Locate every blood parasite and identify its species.
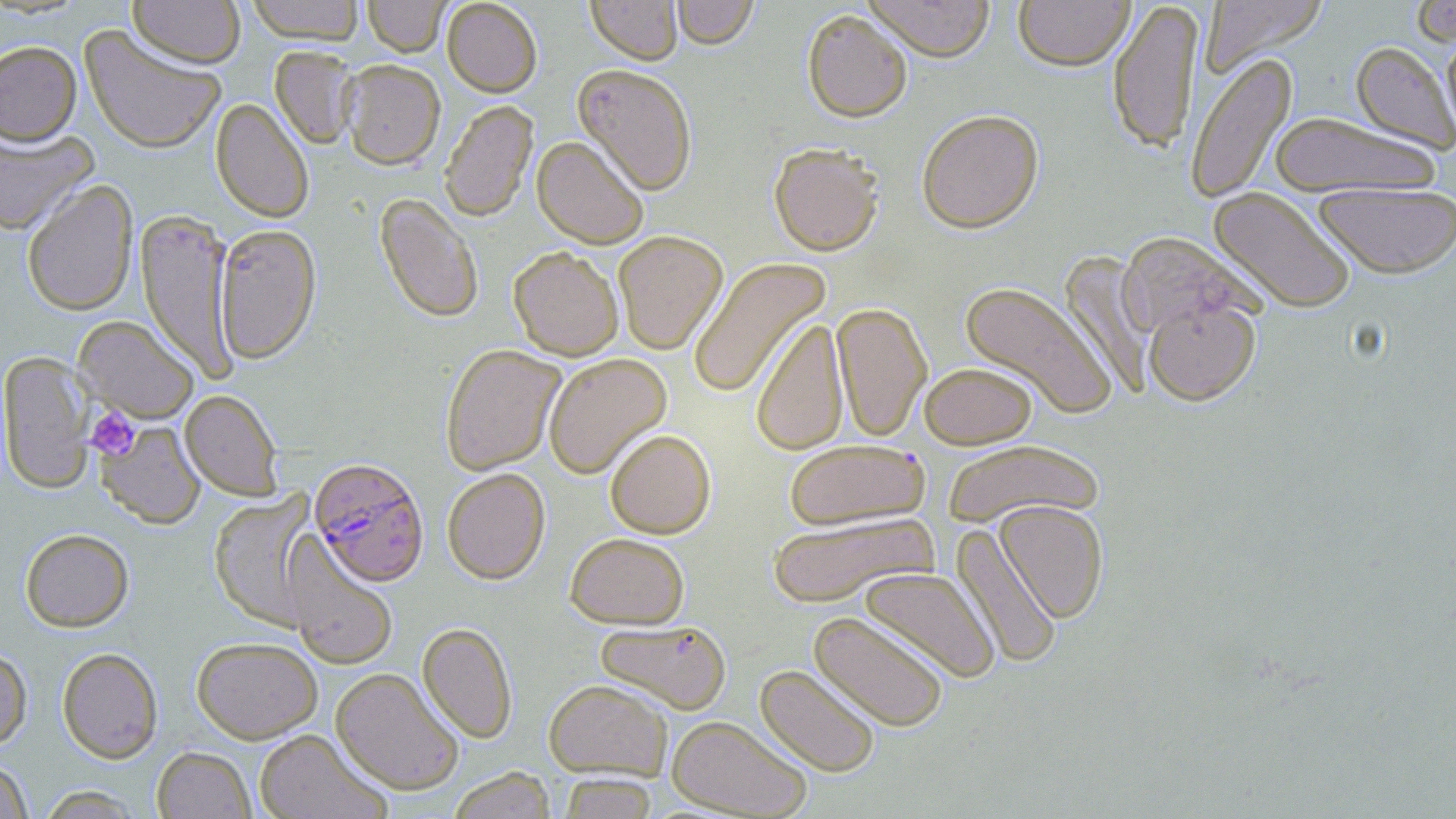
Approximate bounding boxes as named x1/y1/x2/y2 corners in pixels.
Plasmodium falciparum-infected red blood cells: (x1=310, y1=458, x2=429, y2=586).
No Plasmodium ovale, Plasmodium malariae, Plasmodium vivax, Babesia divergens, or Trypanosoma brucei observed.

{
  "slide_level_diagnosis": "Plasmodium falciparum",
  "platelet_locations": "approximate bounding boxes as named x1/y1/x2/y2 corners in pixels: (x1=86, y1=407, x2=139, y2=460)",
  "field_of_view": "one of a larger specimen",
  "stain": "May-Grünwald-Giemsa",
  "uninfected_red_blood_cell_locations": "approximate bounding boxes as named x1/y1/x2/y2 corners in pixels: (x1=128, y1=0, x2=246, y2=68), (x1=245, y1=0, x2=366, y2=43), (x1=363, y1=0, x2=450, y2=57), (x1=442, y1=0, x2=542, y2=97), (x1=586, y1=0, x2=682, y2=65), (x1=671, y1=0, x2=759, y2=49), (x1=862, y1=0, x2=994, y2=62), (x1=1013, y1=0, x2=1134, y2=71), (x1=1199, y1=0, x2=1328, y2=76), (x1=1107, y1=1, x2=1203, y2=155), (x1=1410, y1=1, x2=1456, y2=46), (x1=802, y1=10, x2=912, y2=123), (x1=80, y1=24, x2=225, y2=154), (x1=1440, y1=26, x2=1456, y2=145), (x1=0, y1=40, x2=82, y2=146), (x1=1351, y1=41, x2=1455, y2=153), (x1=270, y1=45, x2=360, y2=149), (x1=1185, y1=51, x2=1297, y2=206), (x1=340, y1=59, x2=446, y2=170), (x1=573, y1=64, x2=698, y2=194), (x1=210, y1=97, x2=314, y2=223), (x1=439, y1=99, x2=538, y2=223), (x1=917, y1=108, x2=1044, y2=233), (x1=1269, y1=111, x2=1441, y2=197), (x1=0, y1=127, x2=97, y2=236), (x1=532, y1=135, x2=649, y2=249), (x1=769, y1=143, x2=885, y2=256), (x1=22, y1=178, x2=138, y2=316), (x1=1313, y1=183, x2=1456, y2=278), (x1=1208, y1=187, x2=1356, y2=314), (x1=375, y1=193, x2=484, y2=323), (x1=136, y1=209, x2=237, y2=380), (x1=213, y1=223, x2=322, y2=363), (x1=613, y1=231, x2=728, y2=354), (x1=1115, y1=231, x2=1260, y2=339), (x1=509, y1=246, x2=624, y2=361), (x1=1059, y1=250, x2=1152, y2=398), (x1=688, y1=256, x2=832, y2=399), (x1=959, y1=280, x2=1116, y2=420), (x1=1144, y1=298, x2=1261, y2=405), (x1=832, y1=302, x2=931, y2=442), (x1=74, y1=315, x2=199, y2=423), (x1=751, y1=317, x2=849, y2=456), (x1=440, y1=344, x2=565, y2=475), (x1=1, y1=351, x2=95, y2=494), (x1=543, y1=353, x2=671, y2=479), (x1=919, y1=362, x2=1037, y2=449), (x1=180, y1=389, x2=284, y2=500), (x1=96, y1=420, x2=205, y2=529), (x1=605, y1=429, x2=716, y2=538), (x1=941, y1=438, x2=1105, y2=529), (x1=784, y1=439, x2=929, y2=531), (x1=442, y1=467, x2=550, y2=584), (x1=209, y1=491, x2=318, y2=630), (x1=994, y1=500, x2=1109, y2=623), (x1=767, y1=512, x2=938, y2=608), (x1=951, y1=523, x2=1061, y2=669), (x1=20, y1=528, x2=134, y2=632), (x1=565, y1=532, x2=689, y2=629), (x1=284, y1=534, x2=399, y2=670), (x1=860, y1=567, x2=999, y2=683), (x1=809, y1=610, x2=949, y2=732), (x1=595, y1=619, x2=732, y2=714), (x1=417, y1=622, x2=518, y2=743), (x1=192, y1=636, x2=322, y2=743), (x1=0, y1=645, x2=33, y2=751), (x1=57, y1=647, x2=163, y2=763), (x1=755, y1=664, x2=881, y2=778), (x1=331, y1=668, x2=465, y2=795), (x1=543, y1=679, x2=673, y2=780), (x1=667, y1=715, x2=812, y2=818), (x1=254, y1=729, x2=391, y2=819), (x1=152, y1=745, x2=255, y2=818), (x1=0, y1=758, x2=33, y2=818), (x1=448, y1=766, x2=555, y2=819), (x1=558, y1=773, x2=658, y2=818), (x1=37, y1=786, x2=144, y2=818)",
  "preparation": "thin blood smear",
  "magnification": "1000x",
  "image_size": "1456×819 pixels",
  "modality": "optical microscopy"
}